Find each white blood cell.
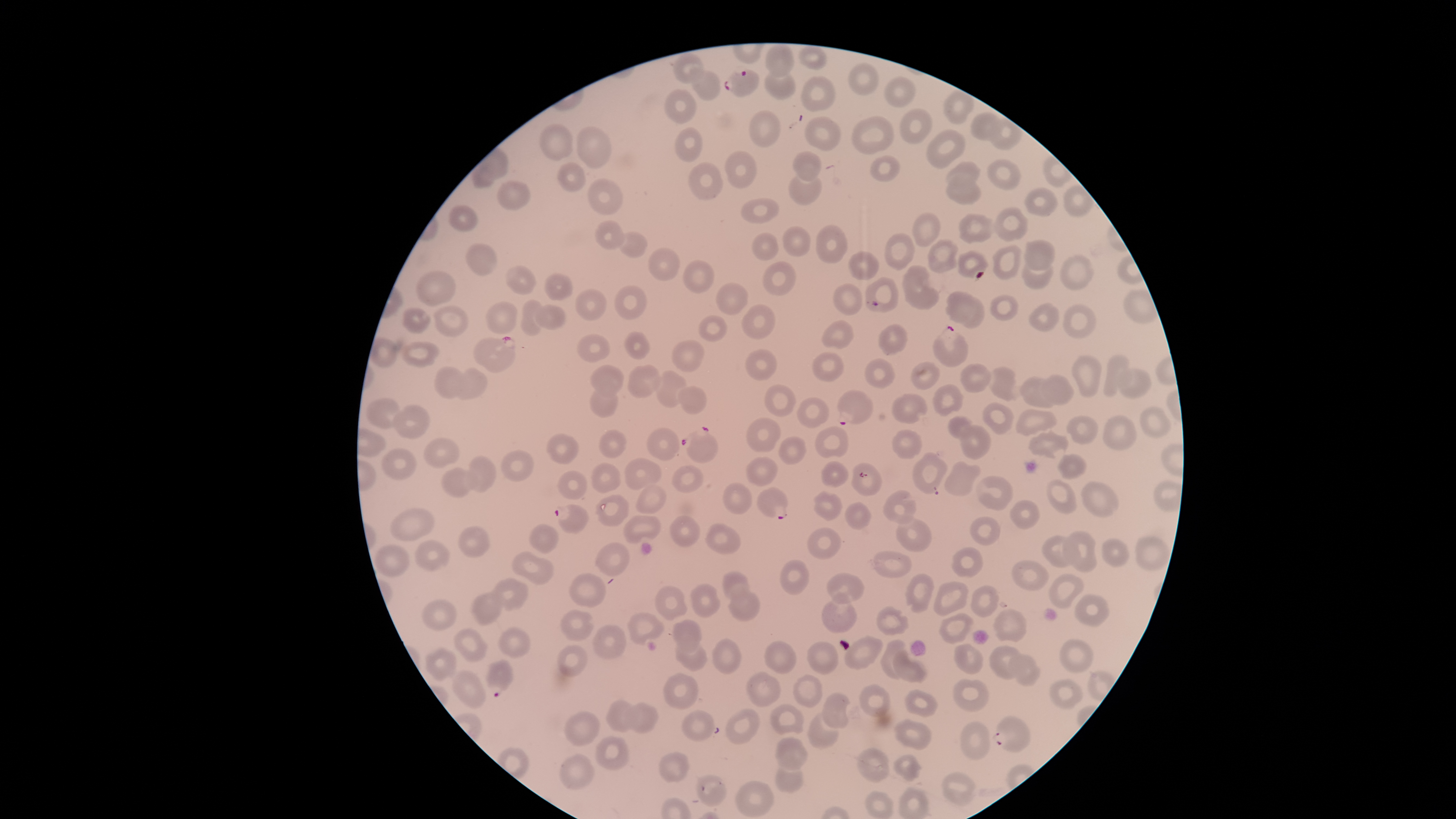
No white blood cells identified.

Approximate bounding boxes as (left, top, right, bottom) in pixels. Parasitized red blood cells: (722, 68, 759, 97), (931, 324, 970, 367), (473, 335, 518, 372), (837, 389, 874, 425), (680, 426, 718, 464), (757, 488, 787, 520), (554, 504, 588, 535), (487, 660, 513, 698), (990, 716, 1031, 752). Uninfected red blood cells: (765, 44, 795, 78), (799, 45, 829, 71), (673, 51, 705, 83), (847, 62, 880, 95), (690, 69, 721, 102), (764, 69, 796, 99), (801, 75, 837, 111), (884, 75, 916, 109), (664, 87, 697, 125), (943, 88, 975, 124), (899, 108, 933, 144), (750, 111, 782, 148), (970, 112, 1003, 140), (851, 115, 895, 155), (804, 116, 842, 152), (989, 117, 1022, 150), (539, 123, 573, 162), (575, 125, 612, 169), (674, 126, 703, 162), (926, 129, 966, 170), (724, 151, 758, 188), (792, 151, 822, 182), (870, 154, 900, 182), (987, 158, 1022, 190), (945, 160, 981, 187), (688, 161, 723, 200), (556, 162, 587, 192), (946, 173, 982, 206), (788, 175, 823, 206), (587, 177, 624, 215), (496, 180, 532, 211), (1062, 185, 1095, 216), (1023, 187, 1058, 217), (740, 198, 780, 224), (449, 204, 478, 230), (993, 207, 1029, 242), (912, 211, 941, 247), (958, 213, 995, 244), (594, 220, 626, 250), (815, 224, 848, 263), (782, 225, 811, 257), (619, 231, 649, 258), (752, 232, 779, 261), (885, 232, 915, 271), (927, 239, 959, 273), (1023, 240, 1056, 272), (465, 242, 498, 275), (992, 244, 1023, 281), (647, 247, 680, 281), (848, 250, 880, 281), (957, 250, 990, 279), (1059, 254, 1094, 290), (683, 258, 716, 293), (762, 261, 796, 296), (1020, 261, 1053, 290), (506, 264, 537, 294), (902, 264, 940, 310), (415, 270, 457, 307), (543, 273, 573, 301), (865, 277, 899, 313), (715, 283, 749, 315), (833, 283, 862, 316), (614, 285, 647, 321), (575, 288, 608, 322), (945, 292, 985, 329), (989, 294, 1018, 321), (520, 299, 545, 336), (485, 301, 517, 334), (433, 303, 470, 338), (1028, 303, 1060, 332), (1063, 303, 1097, 339), (741, 304, 775, 340), (532, 305, 567, 329), (401, 306, 432, 334), (697, 315, 728, 342), (821, 319, 854, 349), (878, 323, 909, 355), (624, 331, 650, 360), (576, 334, 610, 362), (369, 337, 400, 367), (672, 339, 704, 372), (399, 340, 440, 369), (745, 349, 777, 381), (810, 352, 844, 382), (1070, 354, 1102, 397), (1103, 354, 1131, 397), (864, 358, 896, 389), (911, 361, 940, 390), (627, 363, 662, 399), (960, 363, 991, 393), (590, 365, 624, 398), (434, 366, 464, 400), (454, 367, 488, 400), (985, 367, 1019, 402), (655, 369, 688, 408), (1113, 369, 1153, 399), (1040, 373, 1075, 405), (1020, 376, 1056, 409), (764, 383, 796, 417), (932, 384, 965, 417), (677, 386, 707, 415), (588, 388, 618, 418), (891, 392, 929, 424), (797, 397, 830, 428), (365, 398, 401, 428), (982, 401, 1014, 435), (393, 404, 431, 439), (1139, 406, 1172, 438), (1015, 408, 1058, 436), (1066, 414, 1099, 444), (947, 415, 974, 440), (1102, 415, 1138, 451), (746, 417, 782, 452), (959, 424, 991, 460), (814, 426, 849, 459), (646, 427, 681, 461), (891, 428, 923, 460), (598, 429, 628, 459), (1028, 429, 1069, 460), (545, 433, 579, 465), (778, 436, 807, 465), (422, 437, 460, 469), (381, 447, 418, 481), (501, 450, 534, 482), (912, 452, 949, 495), (1056, 453, 1088, 480), (467, 454, 497, 492), (746, 457, 778, 486), (624, 458, 663, 489), (820, 460, 849, 488), (944, 460, 981, 498), (592, 462, 621, 493), (851, 462, 883, 496), (671, 465, 704, 494), (440, 467, 478, 498), (557, 470, 588, 500), (977, 475, 1014, 510), (1047, 478, 1077, 516), (1081, 480, 1120, 518), (723, 481, 753, 515), (635, 484, 667, 514), (883, 490, 917, 525), (813, 491, 843, 521), (595, 493, 630, 526), (1010, 500, 1040, 529), (843, 501, 872, 530), (390, 507, 435, 541), (894, 513, 932, 552), (669, 514, 701, 547), (623, 515, 661, 545), (969, 516, 1001, 547), (704, 523, 742, 554), (529, 524, 558, 554), (457, 526, 491, 558), (807, 527, 841, 559), (1062, 531, 1098, 573), (1041, 534, 1082, 567), (1135, 536, 1171, 571), (1100, 537, 1130, 567), (414, 539, 450, 571), (593, 542, 629, 576), (373, 543, 410, 577), (952, 547, 982, 578), (511, 550, 554, 586), (869, 550, 912, 577), (779, 558, 810, 595), (1011, 560, 1050, 590), (721, 571, 750, 600), (826, 572, 865, 605), (569, 573, 607, 607), (905, 573, 935, 613), (1047, 573, 1084, 609), (493, 577, 529, 612), (933, 581, 969, 616), (690, 583, 721, 618), (970, 584, 999, 618), (654, 585, 688, 621), (729, 589, 761, 621), (471, 590, 504, 626), (821, 591, 858, 633), (1074, 594, 1111, 627), (421, 599, 457, 631), (876, 604, 910, 637), (559, 609, 594, 641), (992, 609, 1027, 642), (628, 612, 666, 646), (939, 612, 974, 645), (672, 620, 703, 653), (593, 624, 627, 659), (497, 626, 531, 658), (454, 627, 489, 663), (844, 635, 884, 669), (712, 638, 741, 674), (674, 639, 709, 672), (880, 639, 910, 680), (1059, 639, 1095, 674), (764, 641, 798, 675), (806, 641, 840, 676), (954, 643, 984, 674), (557, 644, 589, 677), (989, 645, 1021, 680), (424, 646, 457, 681), (892, 649, 928, 683), (1008, 652, 1041, 686), (450, 670, 486, 710), (745, 671, 782, 707), (662, 673, 698, 709), (792, 674, 823, 707), (953, 678, 990, 712), (1049, 678, 1084, 709), (858, 684, 892, 717), (904, 689, 938, 717), (821, 692, 850, 729), (606, 698, 635, 733), (627, 700, 659, 733), (769, 703, 806, 735), (681, 708, 715, 742), (725, 708, 761, 744), (564, 710, 601, 746), (807, 712, 839, 749), (894, 719, 932, 750), (960, 722, 991, 760), (595, 735, 629, 770), (773, 735, 809, 770), (856, 746, 891, 783), (657, 751, 690, 783), (559, 753, 594, 789), (893, 753, 924, 781), (774, 764, 804, 793), (940, 771, 977, 806), (696, 774, 728, 806), (735, 779, 774, 817), (863, 790, 894, 818). Species: Plasmodium falciparum. Single field of view. Circular visible region. Giemsa stain. Thin blood smear. Image is 1456×819 pixels. Presence: malaria parasites identified. Smartphone photograph through the microscope eyepiece.